Comment on the morphology of the red blood cells.
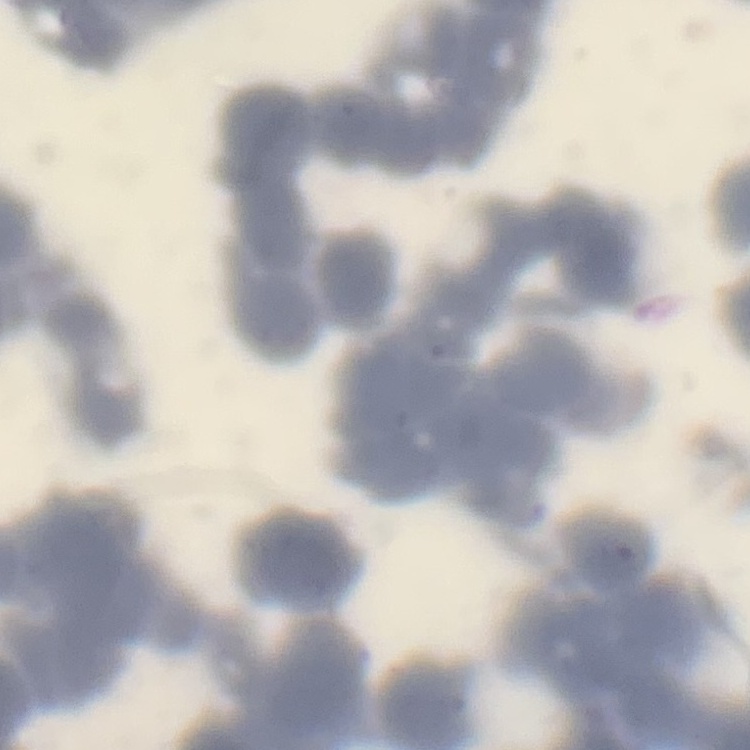

Rouleaux formation.

stain = Field's or Giemsa
image type = square crop of a larger photomicrograph
preparation = thin blood smear